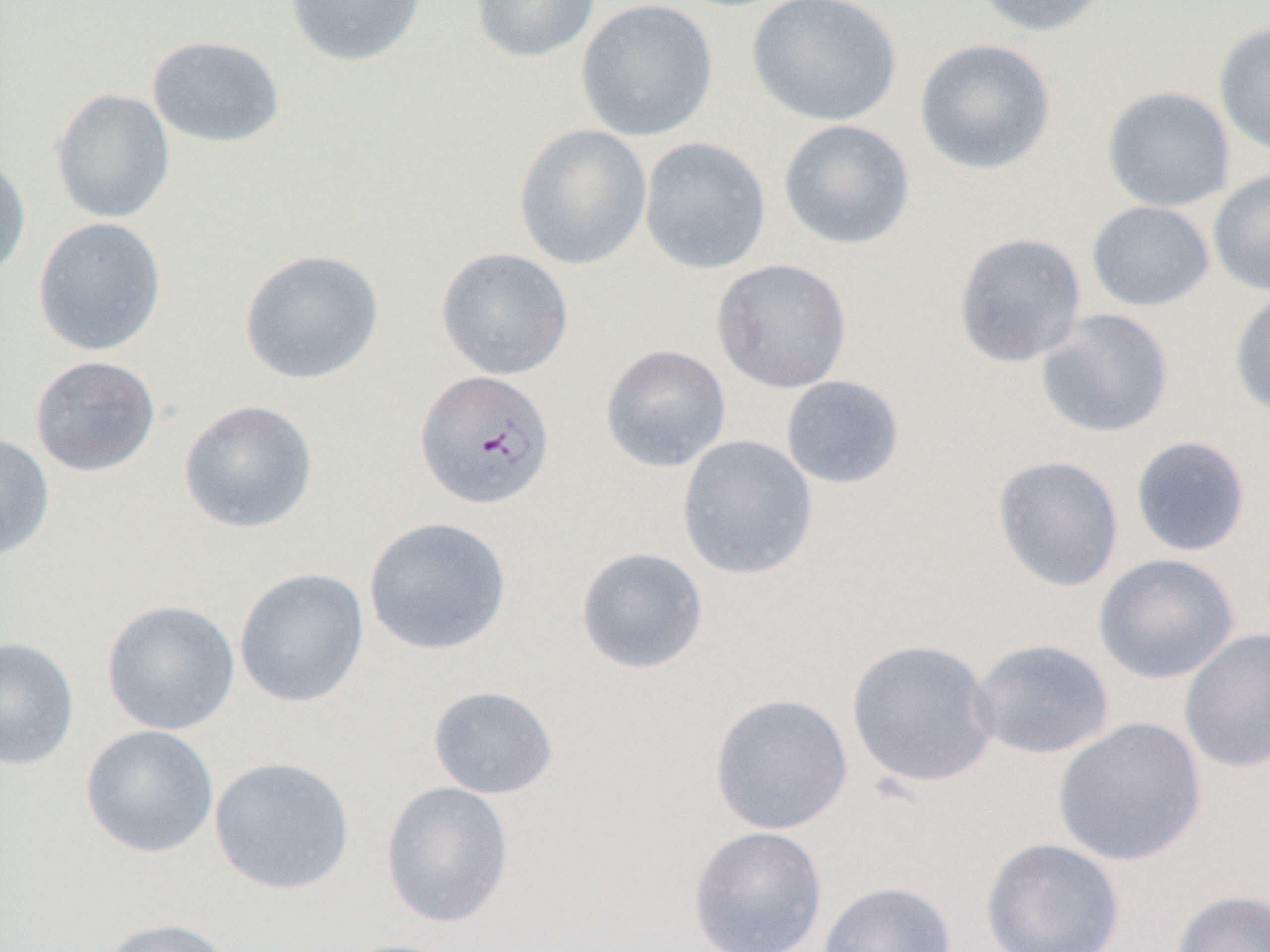

Approximate bounding boxes as (x1,y1)-(x2,y2) corner pairs in pixels. Plasmodium falciparum-infected red blood cell locations: (414,369)-(556,510). Uninfected red blood cell locations: (284,0)-(428,68), (470,0)-(600,63), (576,0)-(719,142), (746,0)-(902,126), (970,0)-(1115,37), (1213,21)-(1270,158), (147,35)-(285,148), (914,38)-(1057,175), (1101,86)-(1236,212), (50,89)-(175,223), (778,119)-(915,250), (513,124)-(652,270), (639,137)-(771,275), (0,151)-(31,283), (1208,167)-(1270,297), (1086,200)-(1215,311), (32,217)-(167,356), (953,232)-(1087,367), (436,246)-(573,380), (239,248)-(385,385), (712,259)-(852,393), (1229,288)-(1270,417), (1035,309)-(1174,438), (600,344)-(731,473), (30,355)-(160,477), (780,375)-(906,490), (178,399)-(319,534), (0,431)-(55,563), (676,435)-(818,581), (1130,435)-(1251,557), (992,455)-(1124,592), (363,516)-(512,656), (575,547)-(709,675), (1094,553)-(1240,684), (234,568)-(370,708), (101,599)-(241,736), (1179,627)-(1270,774), (0,636)-(80,771), (846,638)-(1001,788), (971,638)-(1115,760), (427,685)-(558,799), (709,693)-(854,836), (1053,716)-(1207,867), (80,724)-(219,858), (209,756)-(356,895), (380,780)-(514,929), (687,826)-(828,952), (980,837)-(1125,952), (817,880)-(956,952), (1171,889)-(1270,952), (96,917)-(235,952), (333,937)-(468,952). Slide-level diagnosis: Plasmodium falciparum. Thin blood smear. Light microscopy. Single field of view. 1000x magnification. Image is 1270×952 pixels.